Report the malaria status of this cell.
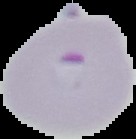

Parasitized.

Segmented cell region on a black background. From a thin blood film. Image is 136×139 pixels.